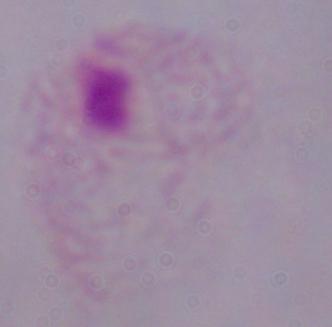

A trichomonad is shown. Micrograph. Captured at 1000x magnification.